Report the malaria status of this cell.
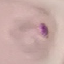

It is parasitized.

preparation = thin smear
stain = Giemsa
image type = cell patch, automatically extracted from a larger field of view and resized to 64 × 64 pixels
capture = smartphone camera at the microscope eyepiece